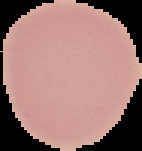

The area outside the segmented cell region is set to black. From a thin blood film. Image is 142×151 pixels. Result: no malaria parasites detected.